Look for Plasmodium parasites.
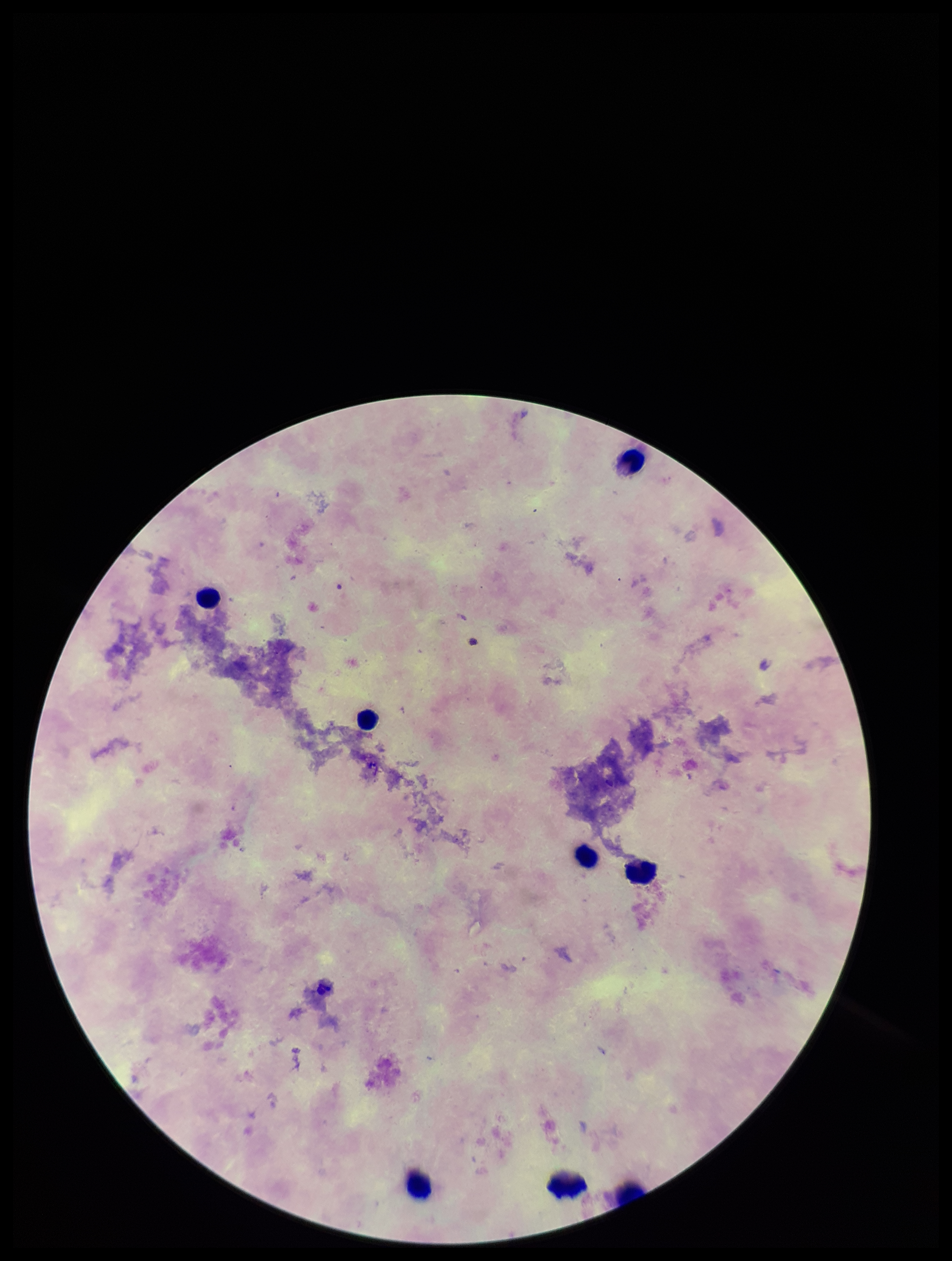
None seen.

Summary:
  - Leukocyte count: 8
  - Stain: Giemsa
  - Preparation: thick smear
  - Field of view: one from this slide
  - Capture: smartphone photograph through the microscope eyepiece
  - Parasite count: 0
  - Patient malaria status: negative
  - Image size: 952×1261 pixels